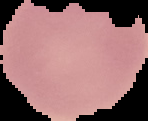
image_type: segmented cell region with the area outside set to black
result: negative for malaria parasites
image_size: 148×121 pixels
preparation: thin blood film